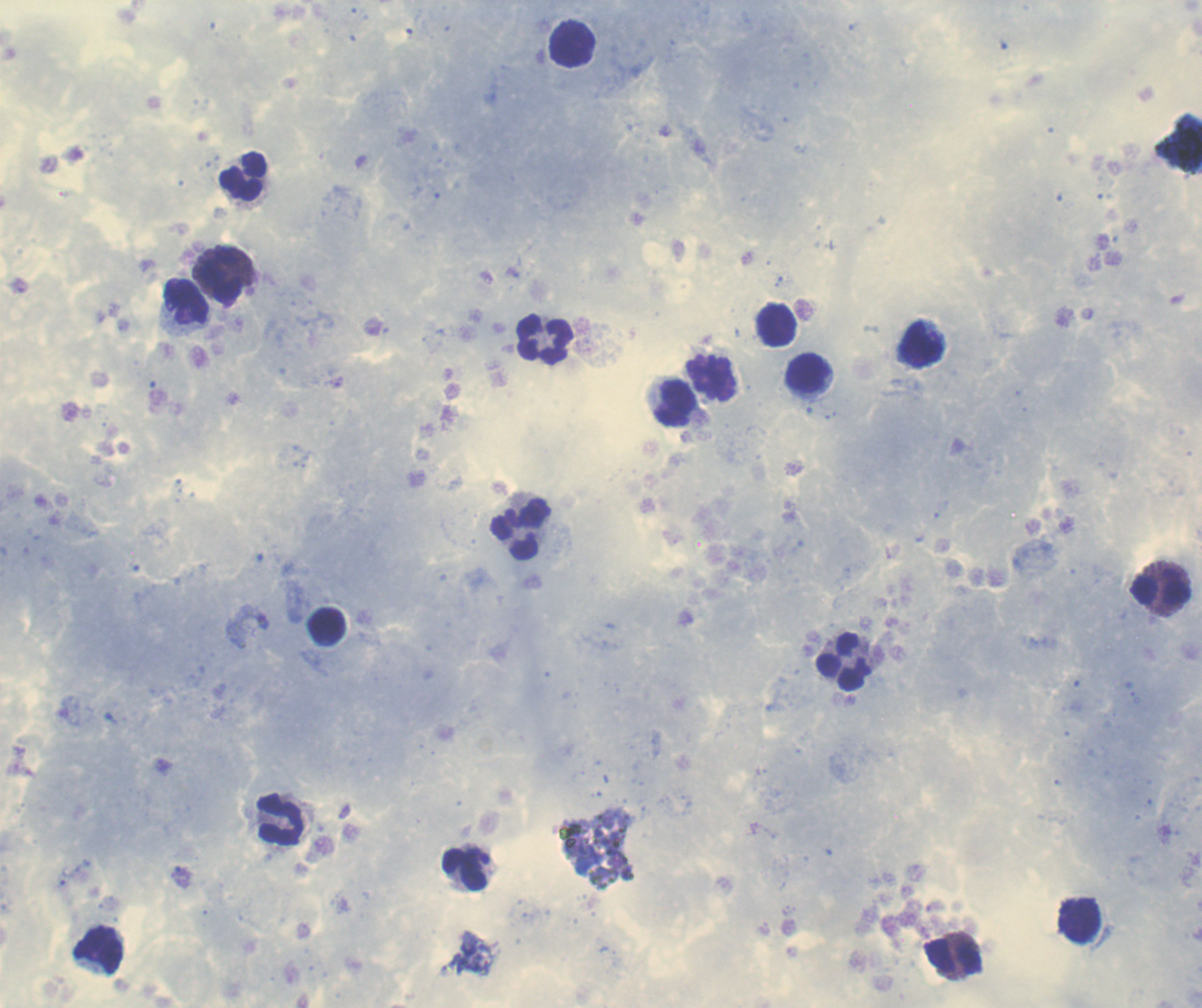

coordinate format = approximate centers as [x, y] in pixels
leukocyte locations = [573, 44], [242, 176], [225, 275], [185, 301], [776, 324], [545, 339], [922, 345], [809, 373], [709, 379], [674, 403], [521, 529], [1159, 590], [325, 625], [845, 662], [280, 819], [464, 868], [1080, 921], [100, 950], [953, 956]
background quality = satisfactory
image size = 1202×1008 pixels
preparation = thick smear of blood
context = previously used in an actual diagnosis
stain = Romanowsky
coloration quality = good
magnification = 100x
field of view = single
result = no malaria parasites detected